Report the malaria status of this cell.
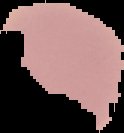
Uninfected.

image type = segmented cell region with the area outside set to black
image size = 124×133 pixels
preparation = thin blood smear